Locate every Plasmodium falciparum-infected red blood cell.
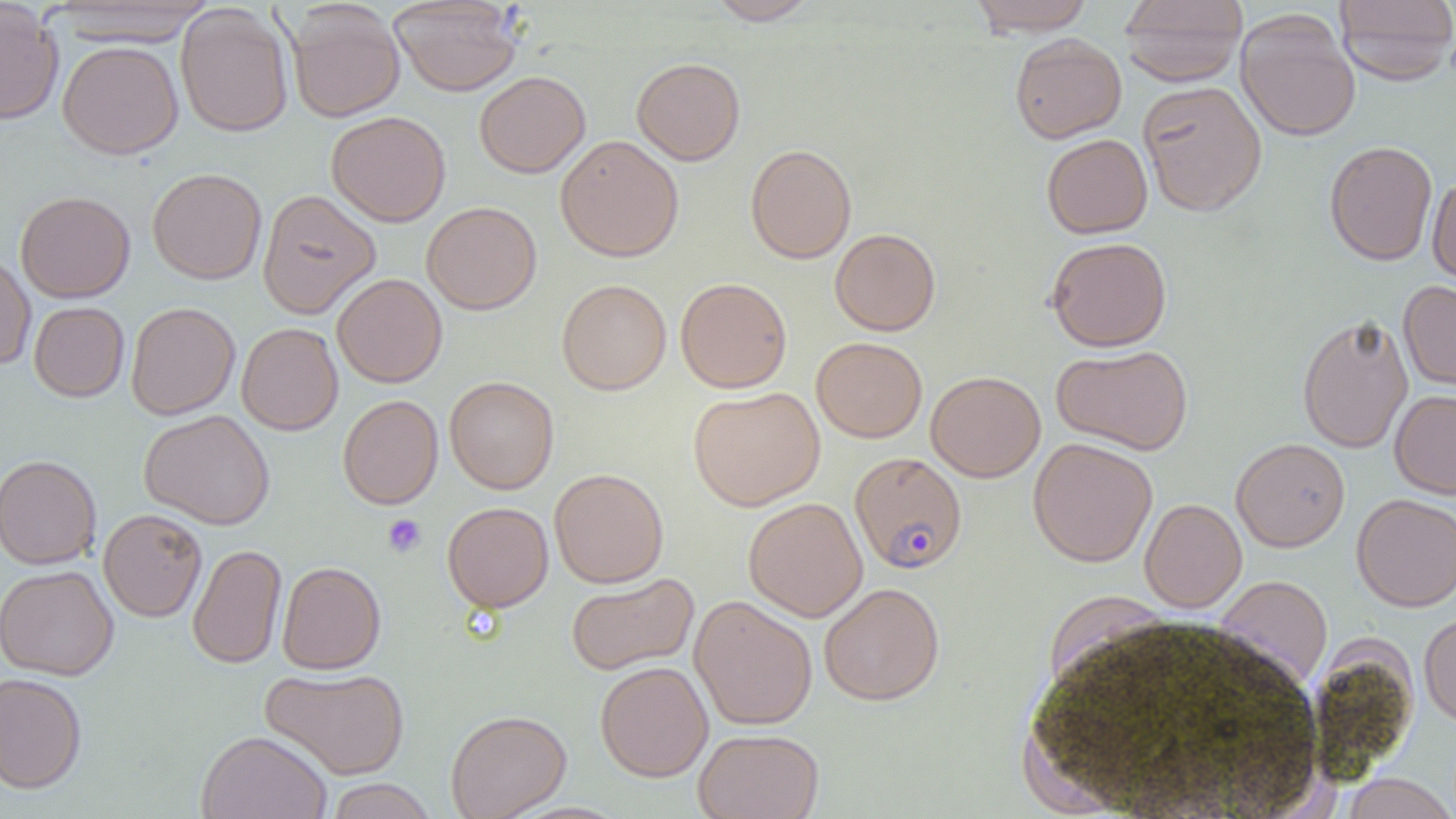
Approximate bounding boxes as [x1, y1, x2, y2] in pixels.
Plasmodium falciparum-infected red blood cells: [850, 451, 968, 574].

Platelet locations: [382, 514, 427, 558]. Uninfected red blood cell locations: [388, 0, 523, 96], [705, 0, 821, 25], [967, 0, 1096, 36], [1119, 0, 1248, 87], [1333, 0, 1456, 85], [0, 1, 64, 125], [43, 1, 219, 45], [287, 3, 406, 123], [175, 5, 293, 137], [1235, 10, 1361, 142], [1010, 33, 1126, 143], [58, 41, 184, 159], [631, 57, 745, 165], [474, 71, 590, 178], [1137, 80, 1267, 217], [326, 110, 451, 227], [555, 134, 684, 262], [1041, 134, 1153, 239], [1324, 141, 1437, 266], [745, 144, 857, 263], [147, 168, 267, 284], [1427, 174, 1456, 291], [257, 189, 381, 319], [15, 191, 135, 303], [421, 201, 542, 315], [829, 228, 940, 336], [1045, 237, 1172, 352], [0, 251, 36, 370], [332, 273, 447, 388], [676, 277, 792, 393], [556, 278, 672, 395], [1398, 281, 1456, 395], [29, 301, 130, 402], [125, 302, 240, 420], [1297, 314, 1413, 454], [236, 322, 343, 436], [811, 336, 927, 442], [1052, 345, 1193, 456], [926, 371, 1045, 482], [444, 376, 559, 494], [688, 386, 825, 510], [1389, 390, 1456, 499], [338, 394, 443, 509], [139, 409, 275, 530], [1028, 437, 1157, 567], [1231, 437, 1350, 552], [0, 454, 102, 570], [549, 468, 668, 588], [1352, 493, 1456, 612], [743, 497, 868, 622], [1139, 498, 1247, 613], [442, 501, 553, 613], [98, 509, 207, 622], [188, 544, 287, 669], [277, 561, 386, 674], [0, 565, 119, 681], [566, 572, 699, 676], [1212, 575, 1333, 693], [818, 582, 944, 705], [689, 595, 817, 731], [1419, 611, 1456, 728], [595, 661, 713, 782], [260, 666, 409, 779], [0, 673, 87, 794], [446, 709, 572, 819], [694, 728, 824, 819], [197, 731, 332, 819], [1340, 774, 1456, 819], [324, 779, 438, 819]. Slide-level diagnosis: Plasmodium falciparum. Thin blood smear. Captured at 1000x magnification. Optical microscopy. One field of a larger specimen. Image is 1456×819 pixels.